Assess this cell for malaria.
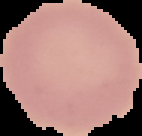
It is uninfected.

image_size: 142×136 pixels
image_type: cell region segmented out of the field of view; surrounding area masked to black
preparation: thin blood smear